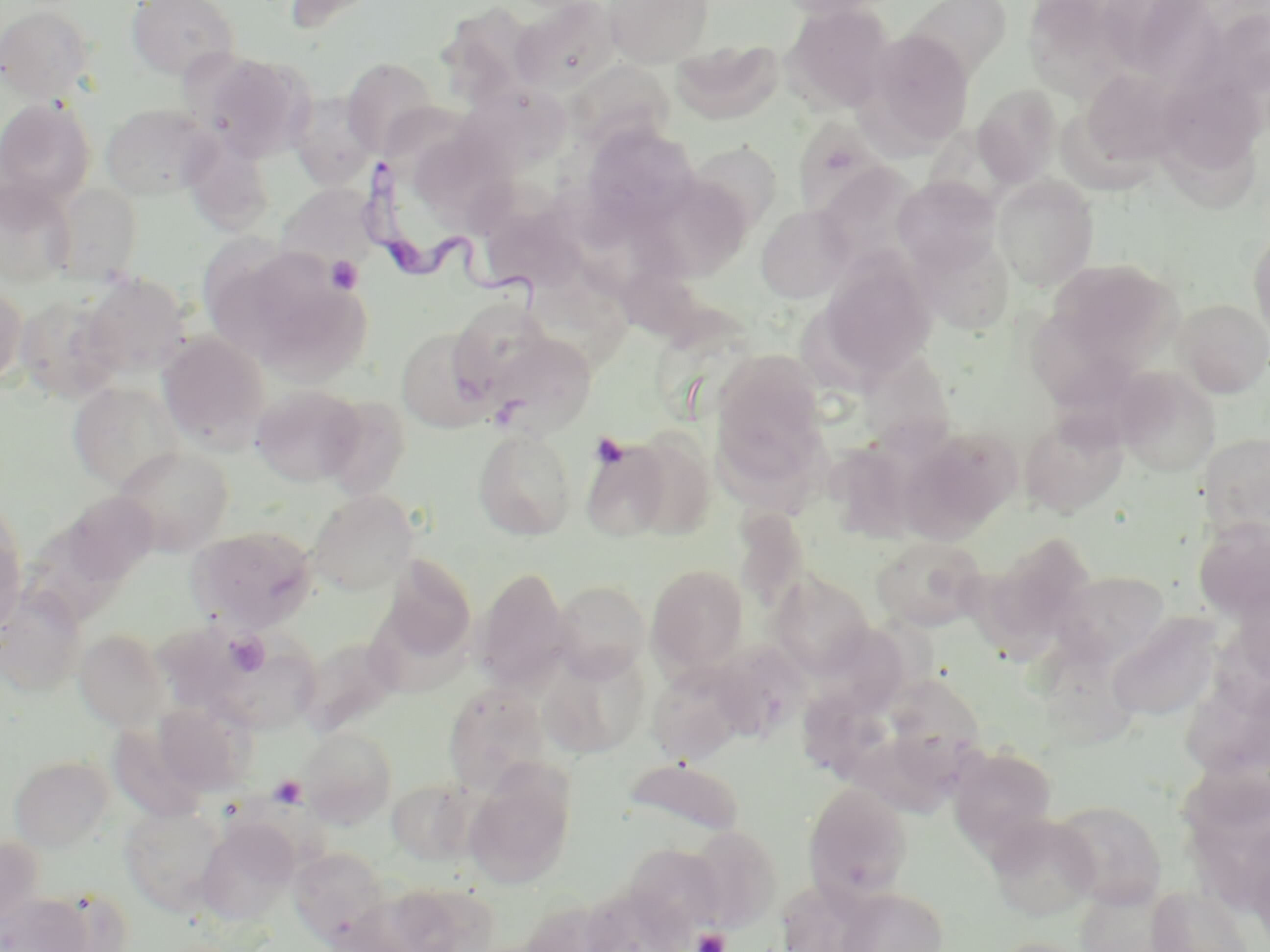

Approximate bounding boxes as (x1,y1)-(x2,y2) corner pairs in pixels. Trypanosoma brucei locations: (355,158)-(552,309). Uninfected red blood cell locations: (126,0)-(239,81), (277,0)-(388,34), (603,0)-(713,68), (774,0)-(893,19), (907,0)-(1011,80), (1023,0)-(1137,102), (1101,0)-(1221,86), (510,1)-(621,97), (0,4)-(96,102), (783,4)-(895,114), (1206,7)-(1270,101), (441,8)-(563,117), (861,28)-(975,151), (669,40)-(783,124), (196,51)-(314,161), (341,57)-(440,158), (1080,68)-(1184,166), (1171,69)-(1262,177), (974,84)-(1063,186), (288,91)-(379,189), (0,99)-(96,209), (100,102)-(217,200), (791,117)-(891,220), (581,123)-(700,235), (1162,124)-(1270,226), (181,132)-(275,236), (685,141)-(782,235), (815,162)-(925,273), (992,175)-(1099,290), (643,176)-(751,281), (892,176)-(1001,273), (0,178)-(75,288), (49,183)-(143,284), (276,183)-(379,275), (756,204)-(855,303), (1248,228)-(1270,344), (913,232)-(1016,336), (817,253)-(937,382), (224,254)-(372,382), (1050,259)-(1183,374), (80,273)-(193,380), (0,281)-(27,390), (16,293)-(123,403), (447,298)-(558,398), (1175,299)-(1270,397), (1031,308)-(1137,419), (396,327)-(495,433), (158,331)-(269,450), (482,331)-(597,439), (861,339)-(964,465), (710,350)-(831,491), (1112,366)-(1220,478), (67,381)-(185,492), (251,385)-(366,486), (319,395)-(411,500), (1019,410)-(1129,516), (902,425)-(1020,537), (473,427)-(577,541), (624,428)-(717,540), (1203,433)-(1270,539), (581,438)-(673,543), (113,446)-(235,555), (833,447)-(936,544), (308,490)-(417,595), (56,491)-(159,591), (733,507)-(810,614), (0,510)-(27,634), (1193,520)-(1270,622), (189,525)-(318,632), (871,535)-(987,631), (381,556)-(477,663), (646,564)-(749,673), (948,564)-(1062,668), (475,567)-(571,692), (1052,571)-(1170,668), (769,572)-(874,680), (551,579)-(650,681), (0,585)-(86,696), (1106,614)-(1223,721), (75,629)-(172,731), (297,636)-(400,736), (209,638)-(322,734), (711,641)-(810,739), (539,648)-(650,757), (647,664)-(747,764), (893,682)-(988,769), (443,684)-(551,795), (1186,686)-(1270,782), (807,694)-(905,782), (155,700)-(256,797), (300,725)-(398,827), (853,737)-(971,823), (949,745)-(1057,852), (9,755)-(113,852), (622,757)-(744,840), (1171,760)-(1270,837), (464,764)-(576,888), (385,779)-(477,866), (803,782)-(912,903), (1052,800)-(1167,909), (120,804)-(228,915), (986,815)-(1101,921), (196,819)-(299,926), (1188,820)-(1270,915), (688,825)-(781,931), (623,843)-(727,942), (290,849)-(391,946), (384,880)-(499,952), (1145,884)-(1254,952), (836,887)-(948,952), (340,889)-(442,952), (2,892)-(94,952), (990,937)-(1094,952). Platelet locations: (325,255)-(364,295), (589,433)-(629,469), (223,631)-(270,676), (269,775)-(307,809), (692,928)-(729,952). Slide-level diagnosis: Trypanosoma brucei. Light microscopy. Thin blood smear. May-Grünwald-Giemsa stain. Image is 1270×952 pixels. Single field of view. 1000x magnification.